Locate and identify every blood parasite.
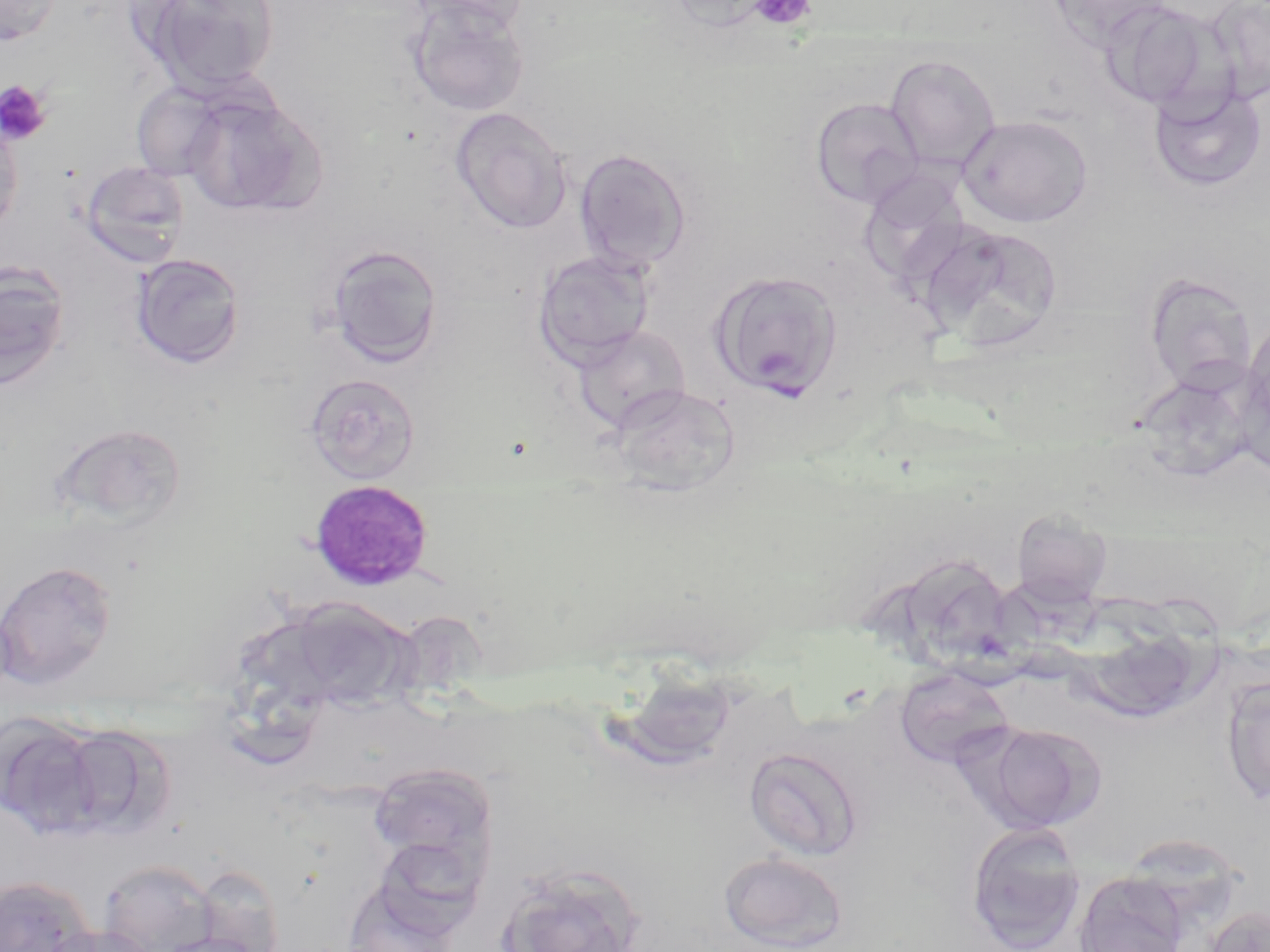
Approximate bounding boxes as (x1, y1, x2, y2) in pixels.
Plasmodium malariae-infected red blood cells: (307, 479, 435, 592).
No Plasmodium falciparum, Plasmodium ovale, Plasmodium vivax, Babesia divergens, or Trypanosoma brucei observed.

slide-level diagnosis = Plasmodium malariae
magnification = 1000x
image size = 1270×952 pixels
stain = May-Grünwald-Giemsa
field of view = single
platelet locations = approximate bounding boxes as (x1, y1, x2, y2) in pixels: (749, 0, 817, 31), (0, 80, 51, 146)
preparation = thin blood film
uninfected red blood cell locations = approximate bounding boxes as (x1, y1, x2, y2) in pixels: (0, 0, 62, 47), (137, 0, 280, 94), (403, 0, 531, 30), (665, 0, 777, 32), (1047, 0, 1174, 50), (1205, 0, 1270, 102), (407, 2, 530, 117), (1099, 2, 1225, 113), (885, 54, 1001, 171), (1148, 82, 1268, 193), (131, 83, 228, 181), (181, 91, 323, 217), (810, 97, 923, 210), (450, 107, 572, 234), (0, 115, 24, 240), (957, 115, 1093, 227), (574, 148, 692, 273), (80, 160, 190, 267), (922, 223, 1066, 353), (320, 244, 443, 368), (532, 249, 655, 369), (131, 253, 245, 368), (0, 261, 72, 391), (709, 269, 844, 401), (1144, 272, 1257, 394), (1243, 313, 1270, 431), (573, 324, 691, 432), (1131, 364, 1259, 485), (305, 373, 421, 485), (609, 384, 741, 497), (50, 422, 188, 532), (1010, 510, 1113, 608), (897, 552, 1016, 669), (0, 559, 117, 690), (278, 595, 419, 714), (894, 667, 1014, 768), (1220, 676, 1270, 804), (0, 712, 106, 839), (975, 721, 1106, 833), (58, 723, 174, 841), (745, 746, 863, 861), (367, 761, 499, 883), (965, 822, 1087, 952), (717, 850, 850, 952), (99, 859, 219, 952), (495, 862, 647, 952), (189, 864, 286, 951), (1073, 871, 1189, 952), (0, 875, 98, 952), (341, 878, 460, 952), (1207, 905, 1270, 952), (46, 923, 158, 952)
modality = light microscopy